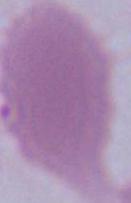
Photomicrograph. 1000x magnification. A red blood cell is shown.